Identify the cell.
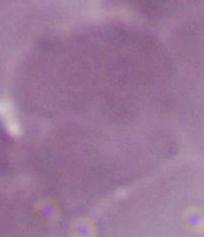
An erythrocyte.

magnification: 1000x
modality: photomicrograph